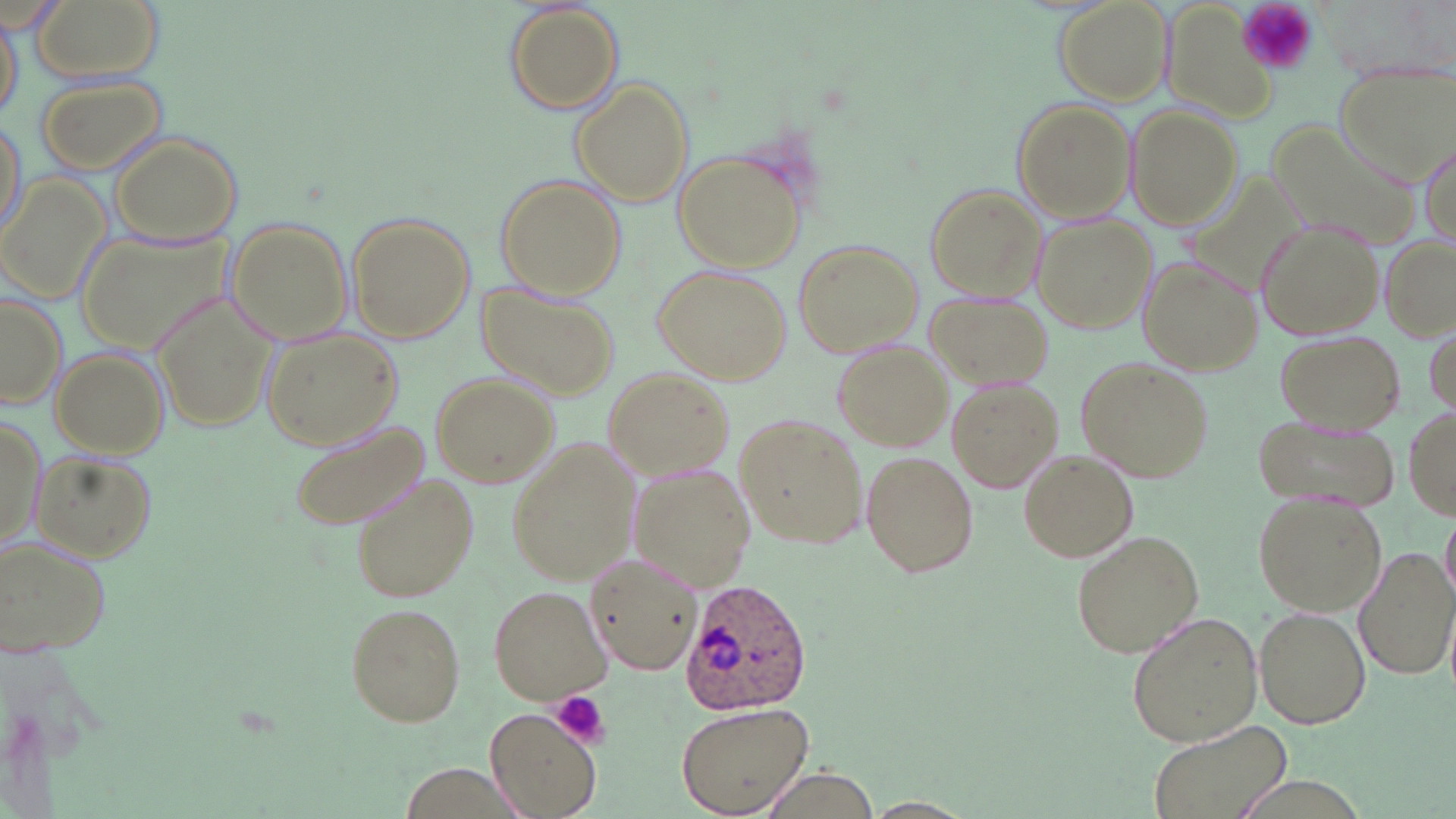
slide-level diagnosis = Plasmodium ovale
field of view = one of a larger specimen
uninfected red blood cell locations = approximate bounding boxes as [x1, y1, x2, y2] in pixels: [31, 0, 162, 83], [1056, 1, 1173, 107], [506, 3, 622, 113], [1155, 8, 1281, 132], [2, 10, 23, 122], [1334, 63, 1456, 184], [34, 75, 167, 179], [571, 80, 693, 206], [1012, 99, 1135, 225], [1129, 106, 1242, 228], [1, 115, 27, 243], [1265, 119, 1422, 252], [109, 131, 244, 247], [1418, 136, 1454, 255], [674, 149, 809, 272], [3, 174, 113, 305], [495, 175, 624, 301], [925, 183, 1046, 302], [346, 212, 473, 342], [1029, 213, 1156, 334], [1254, 217, 1387, 341], [226, 218, 354, 345], [79, 228, 234, 354], [1380, 234, 1456, 342], [794, 240, 923, 359], [1137, 253, 1264, 377], [653, 265, 790, 386], [476, 285, 620, 401], [149, 287, 278, 435], [0, 290, 68, 410], [925, 291, 1054, 392], [260, 326, 403, 449], [1273, 330, 1407, 435], [831, 338, 954, 452], [45, 347, 170, 457], [1073, 355, 1212, 483], [603, 367, 734, 481], [431, 372, 557, 487], [945, 376, 1063, 494], [1406, 406, 1454, 521], [0, 411, 45, 559], [734, 413, 869, 551], [1252, 413, 1397, 510], [284, 414, 431, 529], [508, 437, 643, 586], [1018, 448, 1138, 563], [860, 450, 980, 579], [34, 452, 156, 563], [632, 465, 759, 592], [348, 470, 479, 605], [1251, 491, 1387, 617], [1442, 515, 1456, 602], [1070, 528, 1204, 658], [0, 535, 110, 658], [1355, 546, 1454, 681], [583, 553, 703, 674], [490, 584, 614, 705], [342, 601, 468, 727], [1254, 606, 1371, 729], [1125, 610, 1265, 749], [676, 701, 814, 817], [486, 709, 602, 818], [1153, 726, 1286, 819], [860, 798, 979, 819]
platelet locations = approximate bounding boxes as [x1, y1, x2, y2] in pixels: [1238, 0, 1319, 76], [549, 690, 610, 747]
modality = light microscopy
Plasmodium ovale-infected red blood cell locations = approximate bounding boxes as [x1, y1, x2, y2] in pixels: [680, 579, 811, 716]
preparation = thin blood smear
stain = May-Grünwald-Giemsa
magnification = 1000x
image size = 1456×819 pixels